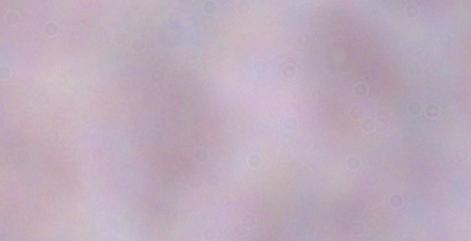
modality = photomicrograph
identification = trypanosome
magnification = 1000x